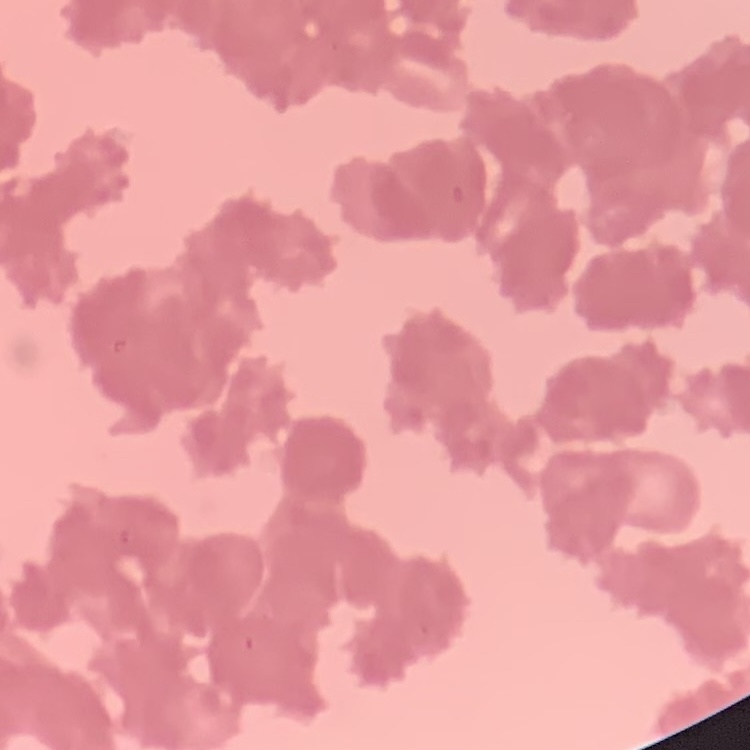
The red blood cells exhibit rouleaux formation. Square crop of a larger photomicrograph. Stained with either Field's or Giemsa. Thin blood smear.